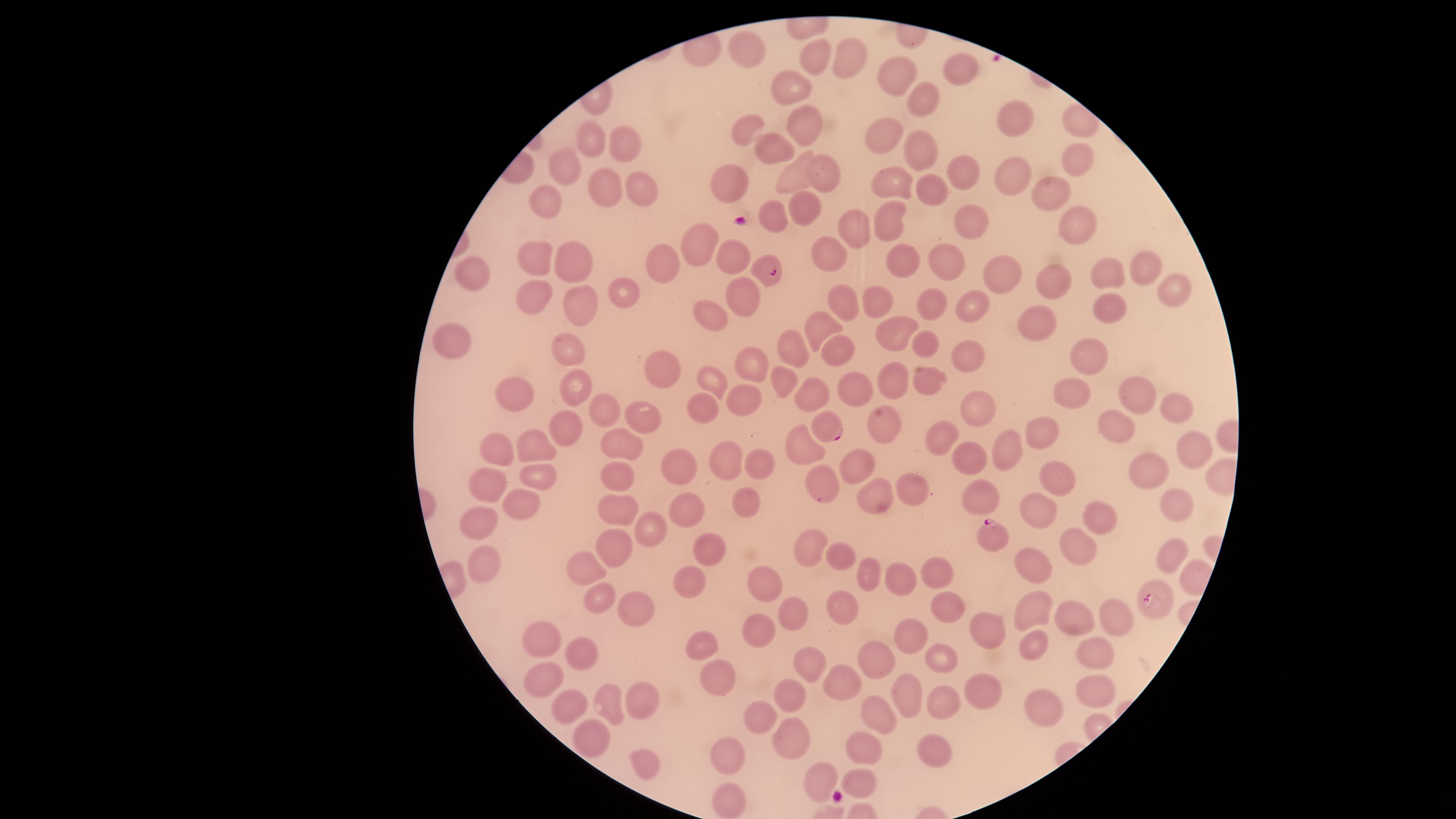

Approximate marker points as {x, y} in pixels.
Summary:
  - Uninfected red blood cells: {751, 50}, {818, 58}, {848, 60}, {960, 69}, {901, 75}, {791, 91}, {921, 98}, {1013, 116}, {807, 118}, {1078, 125}, {748, 129}, {884, 136}, {591, 139}, {624, 145}, {919, 146}, {771, 150}, {1076, 157}, {566, 168}, {821, 168}, {966, 170}, {798, 179}, {1009, 179}, {730, 180}, {895, 184}, {606, 185}, {932, 186}, {1047, 190}, {644, 192}, {549, 198}, {803, 207}, {772, 215}, {966, 223}, {850, 224}, {1074, 224}, {896, 225}, {694, 243}, {733, 252}, {944, 256}, {827, 257}, {537, 258}, {665, 261}, {567, 262}, {905, 262}, {1142, 267}, {1107, 271}, {474, 275}, {1003, 277}, {1051, 278}, {620, 290}, {532, 294}, {1177, 295}, {747, 296}, {843, 301}, {881, 302}, {972, 302}, {931, 303}, {1112, 303}, {579, 305}, {704, 313}, {1040, 321}, {819, 327}, {896, 328}, {447, 340}, {792, 343}, {924, 345}, {570, 351}, {837, 352}, {965, 355}, {1089, 355}, {751, 360}, {657, 367}, {712, 377}, {783, 378}, {896, 381}, {572, 385}, {932, 385}, {856, 392}, {512, 395}, {811, 395}, {1069, 395}, {1134, 395}, {748, 397}, {704, 406}, {603, 408}, {1180, 408}, {979, 411}, {644, 413}, {562, 424}, {881, 424}, {1117, 426}, {1042, 430}, {944, 439}, {802, 442}, {622, 444}, {1195, 449}, {498, 451}, {536, 451}, {1003, 451}, {854, 458}, {967, 458}, {730, 461}, {749, 463}, {675, 467}, {1146, 469}, {620, 473}, {536, 480}, {828, 481}, {1063, 481}, {482, 483}, {879, 492}, {917, 492}, {982, 492}, {514, 503}, {738, 503}, {1175, 505}, {1038, 510}, {616, 511}, {687, 511}, {1101, 520}, {479, 524}, {652, 530}, {1077, 543}, {615, 544}, {712, 547}, {807, 547}, {1166, 555}, {838, 559}, {585, 564}, {483, 566}, {1032, 568}, {935, 569}, {689, 578}, {872, 578}, {906, 579}, {763, 587}, {944, 598}, {603, 599}, {838, 609}, {629, 611}, {1035, 611}, {791, 614}, {1065, 617}, {1114, 620}, {757, 631}, {993, 632}, {917, 634}, {537, 638}, {1028, 643}, {703, 644}, {579, 653}, {874, 653}, {1088, 653}, {940, 659}, {812, 667}, {719, 673}, {536, 679}, {838, 679}, {908, 690}, {1087, 691}, {981, 693}, {790, 695}, {560, 700}, {948, 704}, {606, 705}, {640, 706}, {882, 711}, {1044, 711}, {764, 716}, {588, 735}, {786, 738}, {924, 747}, {865, 749}, {724, 751}, {642, 762}, {855, 782}, {823, 783}, {726, 800}
  - Parasitized red blood cells: {771, 273}, {831, 428}, {993, 532}, {1156, 598}
  - Stain: Giemsa
  - Species: Plasmodium falciparum
  - Visible region: circular
  - Field of view: single
  - Image size: 1456×819 pixels
  - Capture: smartphone photograph through the microscope eyepiece
  - Presence: malaria parasites identified
  - Preparation: thin blood smear